Classify this cell by malaria status.
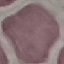
It is uninfected.

Giemsa stain. Automatically extracted cell patch, resized to 64 × 64 pixels. Thin blood smear. Photographed with a smartphone camera at the microscope eyepiece.